Comment on the morphology of the red blood cells.
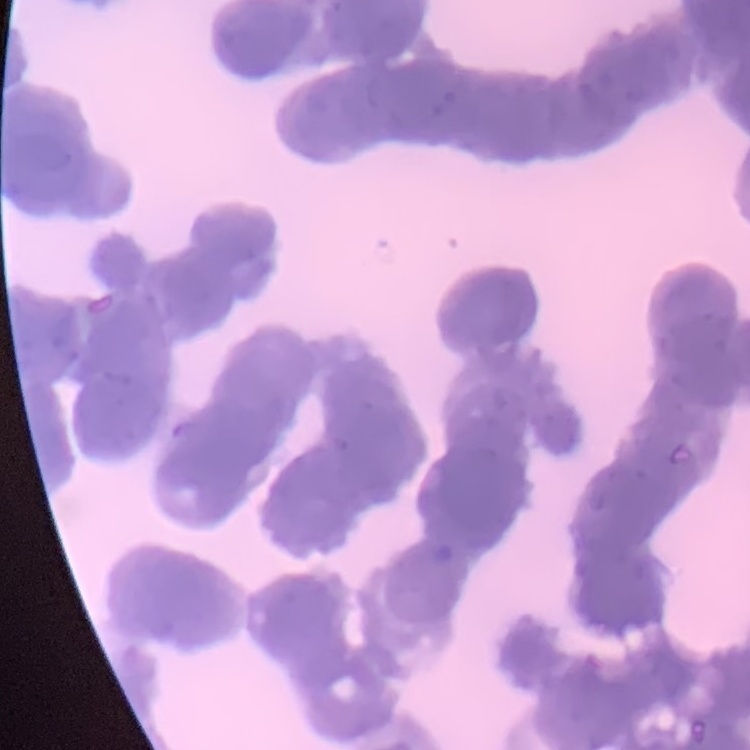

They show rouleaux formation.

Summary:
  - Stain: Field's or Giemsa
  - Image type: one tile cut from a larger photomicrograph
  - Preparation: thin peripheral smear